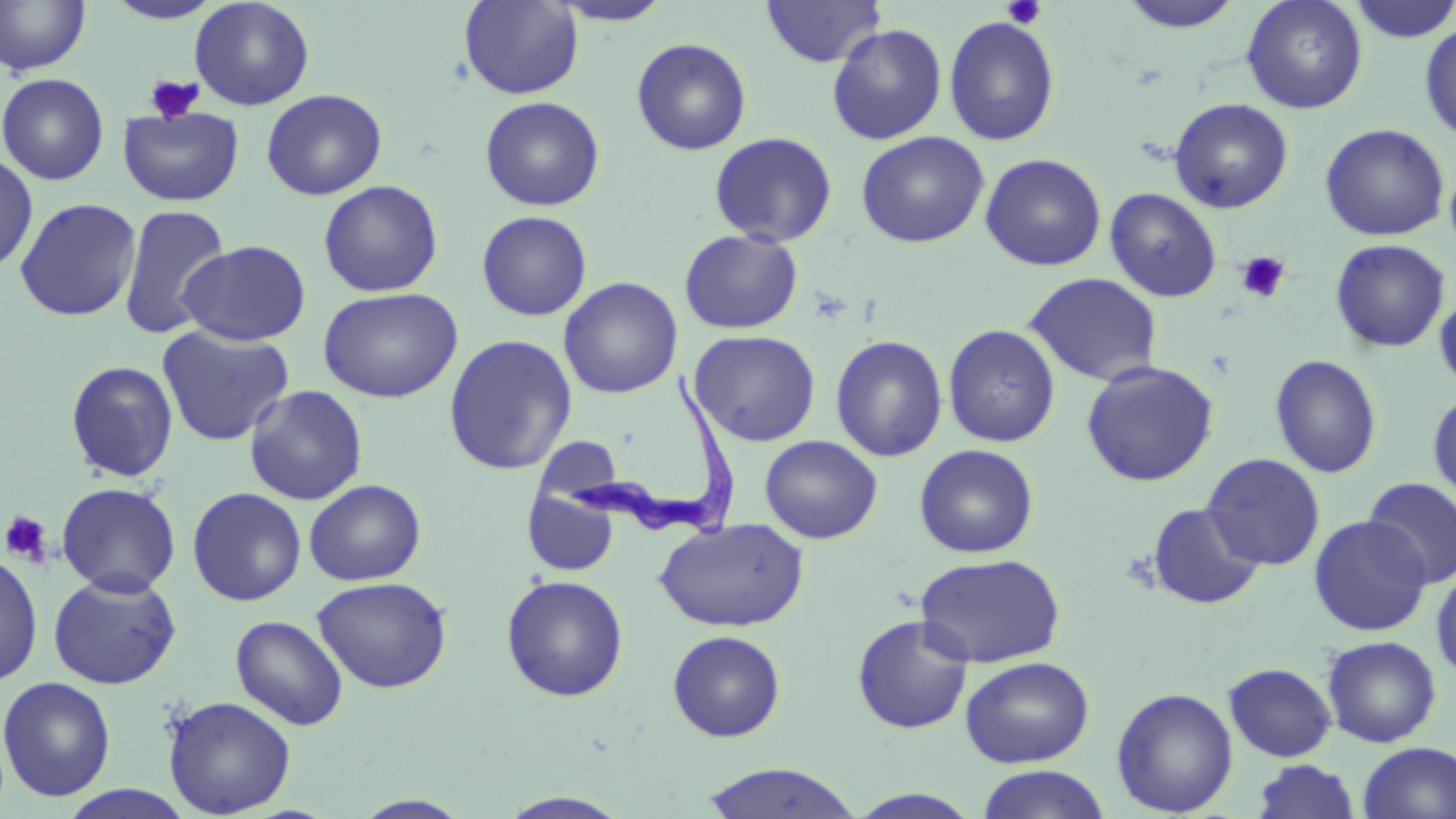
Summary:
  - Coordinate format: approximate bounding boxes as (x1,y1)-(x2,y2) corner pairs in pixels
  - Trypanosoma brucei locations: (558,371)-(745,539)
  - Platelet locations: (1001,0)-(1047,30), (144,75)-(204,123), (1236,250)-(1291,303), (1,510)-(53,565)
  - Uninfected red blood cell locations: (0,0)-(92,76), (104,0)-(223,24), (189,0)-(315,111), (459,0)-(583,100), (761,0)-(886,68), (1117,0)-(1245,34), (1241,0)-(1368,114), (1347,0)-(1456,43), (548,1)-(675,26), (943,15)-(1061,146), (1419,21)-(1456,142), (826,23)-(948,145), (631,37)-(752,156), (0,72)-(109,185), (261,88)-(387,200), (479,96)-(605,211), (1169,97)-(1294,213), (118,106)-(244,206), (1319,123)-(1450,241), (856,130)-(990,248), (708,131)-(838,247), (0,151)-(38,275), (980,153)-(1106,271), (1445,162)-(1456,259), (318,180)-(443,297), (1104,187)-(1222,302), (14,197)-(142,322), (117,203)-(231,340), (476,210)-(592,321), (679,229)-(804,334), (1329,238)-(1451,352), (178,240)-(311,346), (1023,272)-(1163,386), (558,276)-(683,399), (317,286)-(463,403), (1434,291)-(1456,395), (942,323)-(1061,447), (156,325)-(294,447), (689,329)-(821,447), (443,334)-(578,475), (830,334)-(948,462), (1270,354)-(1383,479), (1080,359)-(1219,487), (65,360)-(179,483), (244,385)-(368,505), (1427,391)-(1456,507), (759,435)-(883,543), (914,444)-(1039,558), (1202,453)-(1325,571), (1362,478)-(1456,588), (304,479)-(426,586), (56,482)-(182,596), (187,486)-(307,606), (522,486)-(621,577), (1146,502)-(1266,610), (1308,515)-(1431,636), (654,518)-(808,632), (0,550)-(43,687), (915,552)-(1066,668), (1431,563)-(1456,683), (47,571)-(182,690), (501,574)-(629,702), (312,576)-(452,693), (230,614)-(349,730), (852,614)-(975,734), (667,630)-(787,742), (1322,635)-(1442,748), (960,656)-(1094,768), (1223,662)-(1337,762), (0,675)-(117,802), (1112,686)-(1238,817), (162,695)-(297,818), (1358,741)-(1456,819), (1252,759)-(1361,819), (699,762)-(864,819), (976,765)-(1112,819), (56,785)-(199,819), (848,787)-(984,817), (496,791)-(635,818), (351,794)-(475,818)
  - Slide-level diagnosis: Trypanosoma brucei
  - Image size: 1456×819 pixels
  - Stain: May-Grünwald-Giemsa
  - Field of view: single
  - Preparation: thin blood film
  - Modality: light microscopy
  - Magnification: 1000x